Outline each Plasmodium falciparum-infected red blood cell.
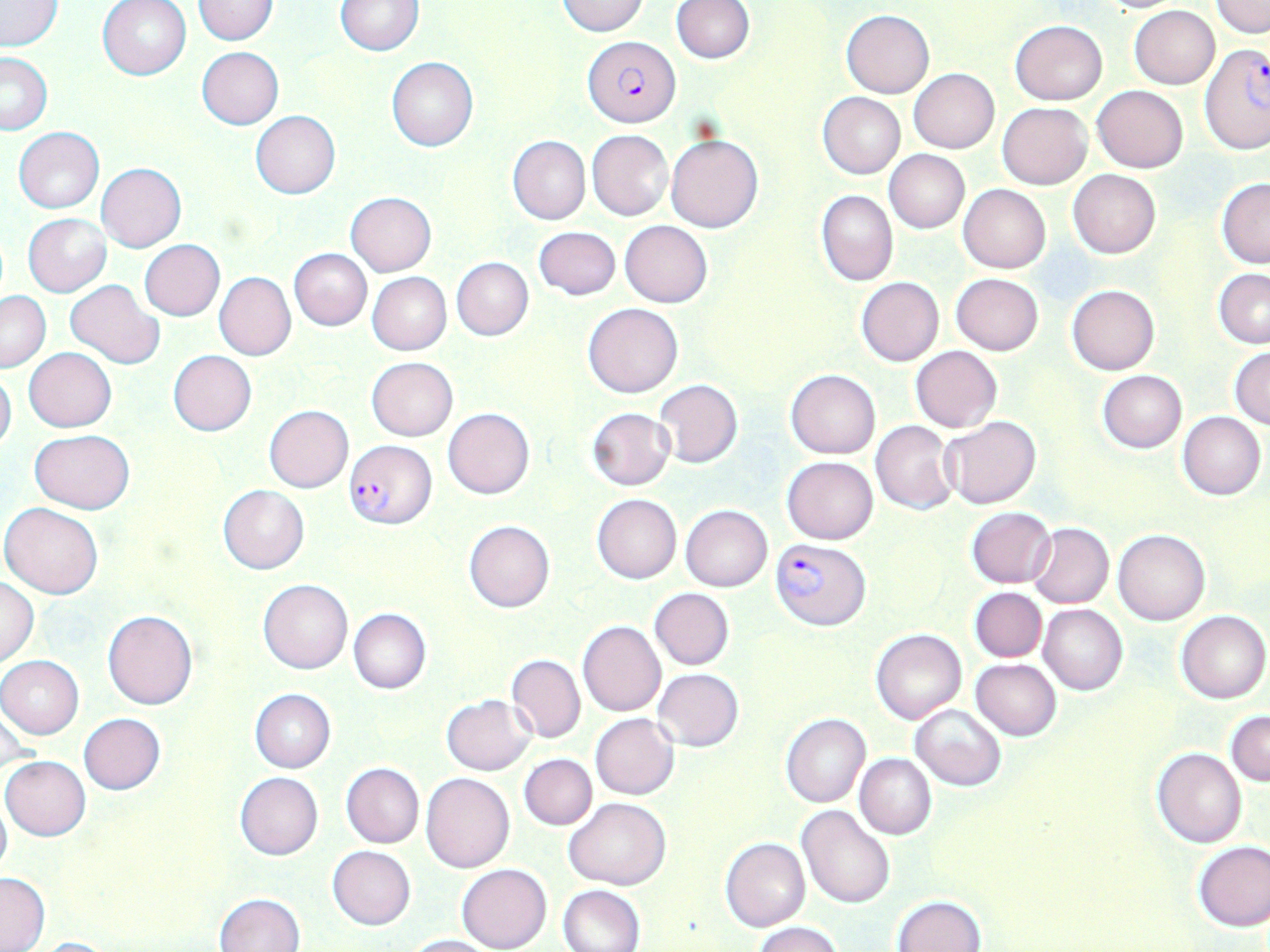

Approximate bounding boxes as (x1, y1, x2, y2) in pixels.
Plasmodium falciparum-infected red blood cells: (582, 37, 680, 127), (1200, 46, 1269, 153), (344, 438, 436, 528), (770, 538, 871, 630).

slide-level diagnosis = Plasmodium falciparum
modality = optical microscopy
uninfected red blood cell locations = approximate bounding boxes as (x1, y1, x2, y2) in pixels: (97, 0, 192, 81), (193, 0, 279, 45), (672, 0, 755, 63), (1092, 0, 1188, 14), (1, 1, 63, 51), (336, 1, 422, 55), (558, 1, 647, 36), (1211, 1, 1270, 36), (1129, 6, 1219, 89), (841, 10, 934, 97), (1011, 21, 1106, 104), (196, 47, 284, 129), (0, 52, 53, 134), (386, 57, 478, 152), (909, 70, 998, 152), (1092, 85, 1189, 173), (818, 91, 905, 178), (998, 103, 1091, 189), (250, 110, 340, 199), (13, 127, 104, 214), (588, 129, 674, 220), (508, 135, 590, 224), (665, 135, 765, 233), (883, 150, 969, 234), (97, 162, 186, 252), (1068, 169, 1160, 258), (1216, 178, 1270, 267), (958, 183, 1050, 273), (816, 190, 898, 287), (347, 191, 436, 276), (23, 214, 110, 297), (620, 221, 712, 307), (533, 226, 620, 301), (139, 240, 225, 321), (289, 249, 371, 330), (451, 257, 534, 341), (1213, 268, 1270, 348), (367, 272, 451, 355), (215, 273, 295, 360), (950, 273, 1043, 355), (856, 277, 943, 366), (66, 280, 164, 368), (1067, 285, 1159, 374), (0, 290, 50, 372), (583, 302, 684, 399), (910, 345, 1003, 432), (1229, 346, 1270, 429), (24, 347, 115, 432), (168, 350, 256, 436), (367, 357, 457, 440), (0, 367, 16, 454), (785, 370, 880, 459), (1096, 370, 1187, 452), (655, 380, 743, 468), (264, 405, 353, 493), (587, 407, 676, 490), (443, 408, 534, 499), (1177, 411, 1266, 501), (941, 416, 1041, 509), (871, 420, 959, 515), (29, 429, 134, 514), (782, 456, 877, 544), (219, 486, 309, 573), (592, 494, 681, 583), (1, 501, 104, 599), (680, 505, 772, 592), (966, 506, 1057, 588), (464, 521, 555, 612), (1028, 523, 1114, 608), (1114, 528, 1210, 625), (1, 577, 39, 668), (258, 580, 352, 674), (648, 587, 735, 670), (970, 588, 1047, 661), (615, 594, 735, 720), (1039, 604, 1127, 695), (102, 609, 198, 710), (349, 609, 430, 694), (1176, 610, 1270, 703), (578, 621, 666, 717), (871, 629, 966, 725), (505, 653, 585, 744), (1, 656, 83, 739), (971, 658, 1061, 740), (653, 668, 744, 751), (249, 689, 335, 773), (442, 694, 535, 774), (910, 702, 1006, 790), (1226, 711, 1270, 786), (78, 713, 166, 795), (590, 713, 680, 800), (781, 713, 871, 807), (1153, 748, 1247, 848), (520, 754, 598, 829), (855, 754, 936, 840), (1, 756, 91, 841), (341, 763, 424, 847), (235, 772, 323, 860), (421, 773, 514, 874), (0, 795, 11, 883), (564, 797, 669, 891), (797, 805, 895, 908), (721, 838, 811, 931), (1193, 840, 1270, 931), (327, 845, 416, 929), (457, 865, 551, 952), (0, 872, 49, 950), (558, 884, 645, 952), (215, 892, 305, 952), (892, 895, 985, 952), (753, 922, 841, 952), (402, 934, 500, 952), (31, 937, 122, 951)
field of view = one of a larger specimen
preparation = thin blood smear
image size = 1270×952 pixels
magnification = 1000x
stain = May-Grünwald-Giemsa